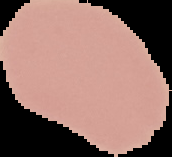
Summary:
  - Image size: 172×157 pixels
  - Malaria status: uninfected
  - Preparation: thin blood smear
  - Image type: segmented cell region on a black background